State which parasite is depicted.
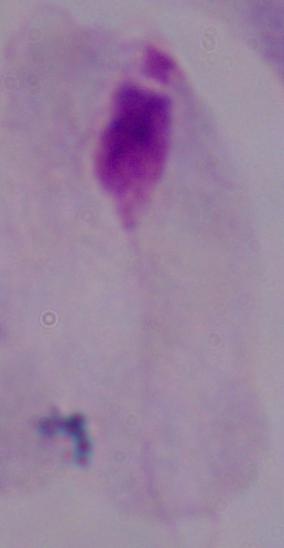
This is a trichomonad.

{
  "modality": "micrograph",
  "magnification": "1000x"
}